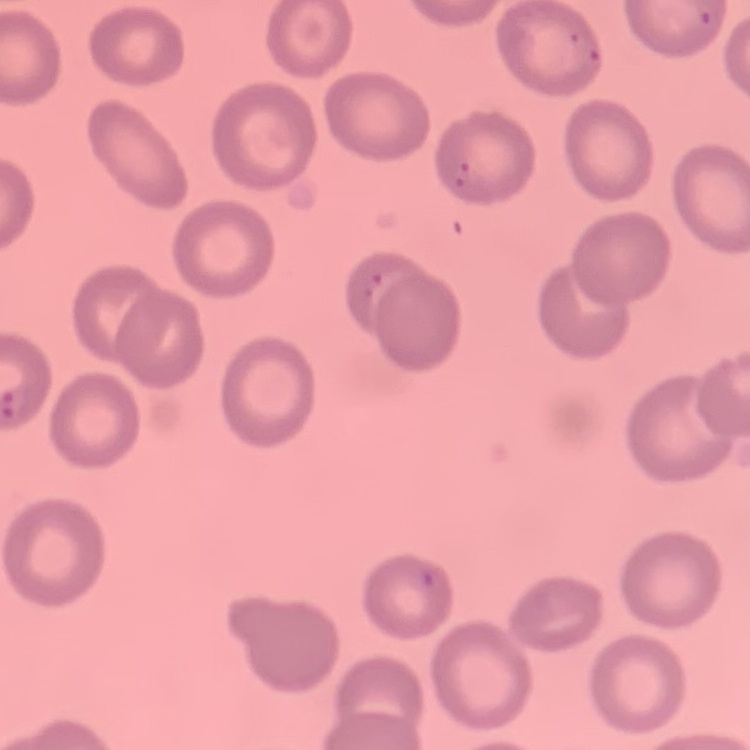

{
  "red_blood_cell_morphology": "no rouleaux formation",
  "image_type": "square crop of a larger photomicrograph",
  "preparation": "thin blood smear",
  "stain": "Field's or Giemsa"
}